Assess for malaria.
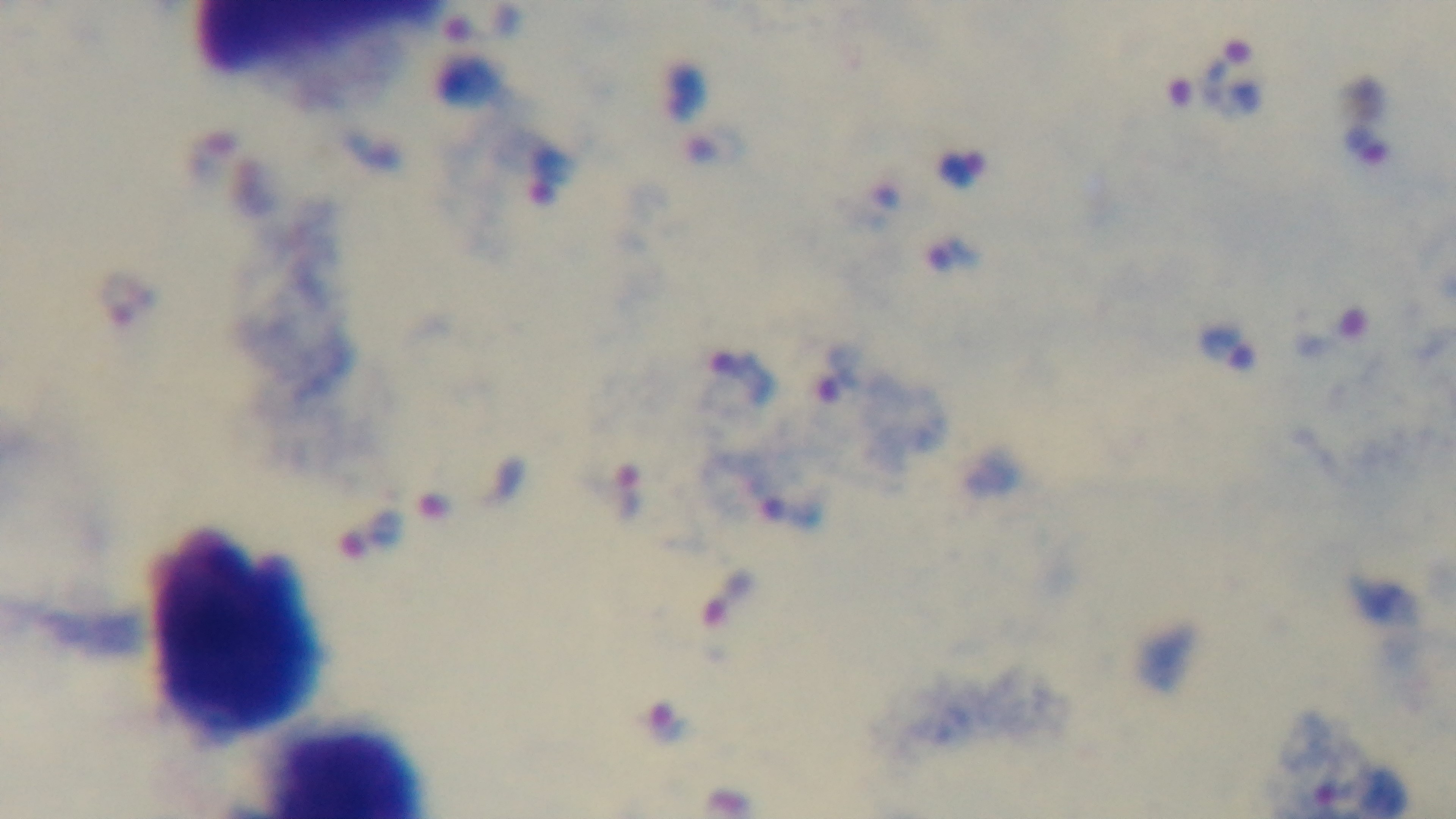
Positive.

Preparation: thick smear. Single field of view. Giemsa-stained. 100x oil-immersion objective. Light microscopy. Captured with a mounted 4K digital camera.